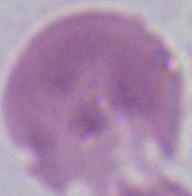

{
  "modality": "micrograph",
  "magnification": "1000x",
  "identification": "red blood cell"
}